Identify the parasite.
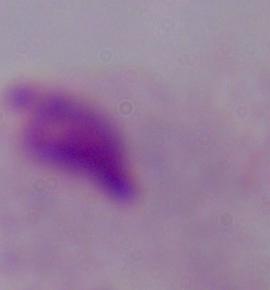
A trichomonad.

Captured at 1000x magnification. Photomicrograph.